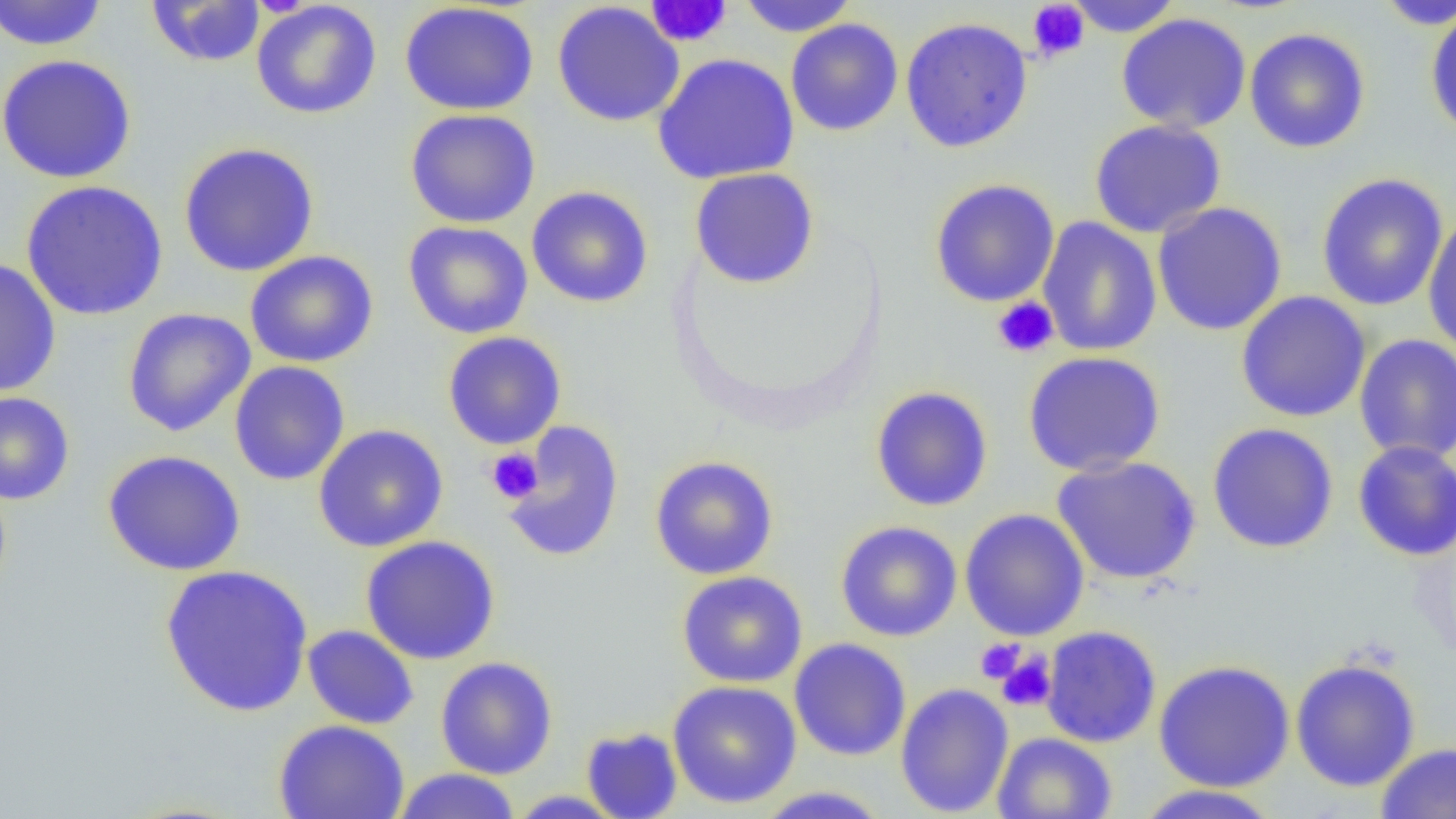

Approximate bounding boxes as [x1, y1, x2, y2] in pixels. Platelet locations: [645, 0, 733, 48], [1027, 1, 1090, 62], [992, 297, 1059, 358], [485, 448, 543, 504], [975, 638, 1025, 684], [995, 651, 1056, 712]. Uninfected red blood cell locations: [0, 0, 109, 51], [737, 0, 859, 37], [1065, 0, 1184, 37], [1373, 0, 1455, 29], [146, 1, 266, 67], [251, 1, 382, 120], [399, 2, 539, 116], [552, 2, 685, 127], [1425, 7, 1456, 140], [1116, 13, 1252, 134], [899, 16, 1034, 153], [786, 18, 903, 137], [1244, 28, 1371, 153], [652, 53, 800, 185], [0, 54, 137, 184], [404, 108, 541, 229], [1089, 119, 1226, 239], [178, 142, 319, 278], [689, 167, 819, 289], [1315, 173, 1449, 311], [929, 178, 1060, 307], [20, 180, 169, 321], [526, 186, 654, 308], [1151, 201, 1288, 336], [1422, 214, 1456, 356], [1037, 216, 1162, 356], [403, 221, 533, 339], [245, 250, 379, 368], [0, 258, 61, 398], [1235, 291, 1371, 423], [121, 307, 256, 437], [442, 331, 567, 449], [1354, 334, 1456, 463], [1023, 351, 1166, 476], [229, 361, 350, 485], [870, 386, 994, 511], [0, 392, 75, 505], [502, 419, 625, 562], [1207, 422, 1339, 553], [312, 424, 449, 552], [1352, 440, 1456, 561], [102, 449, 246, 576], [649, 455, 779, 580], [1051, 455, 1202, 585], [959, 508, 1090, 642], [835, 520, 962, 642], [360, 535, 500, 665], [159, 564, 314, 718], [676, 570, 808, 688], [302, 625, 419, 730], [1041, 625, 1162, 748], [789, 638, 912, 761], [435, 656, 558, 780], [1289, 657, 1421, 792], [1153, 659, 1295, 792], [667, 680, 802, 809], [895, 683, 1014, 817], [273, 719, 410, 819], [581, 726, 683, 818], [991, 732, 1118, 819], [1376, 741, 1456, 819], [392, 768, 522, 818], [1132, 785, 1283, 819], [751, 786, 893, 818], [506, 790, 628, 818]. Slide-level diagnosis: no evidence of blood parasites. One field of a larger specimen. Thin blood film. 1000x magnification. Image is 1456×819 pixels. Optical microscopy.